Name the parasite shown.
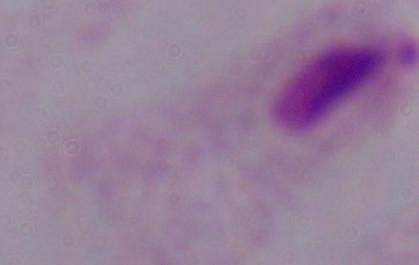

This is a trichomonad.

{
  "modality": "micrograph",
  "magnification": "1000x"
}